Name the blood parasite species.
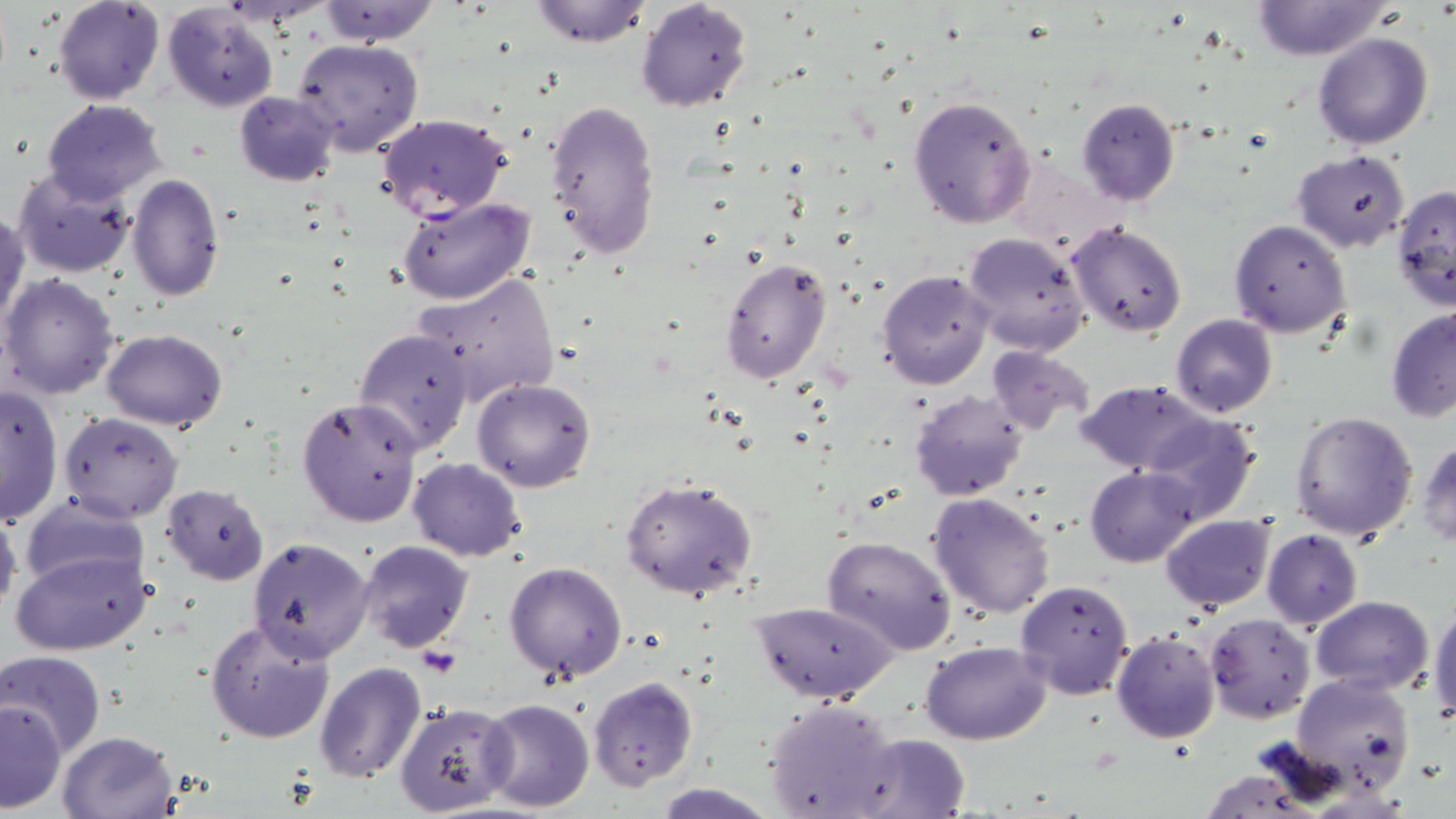

Plasmodium falciparum.

{
  "modality": "optical microscopy",
  "plasmodium_falciparum_infected_red_blood_cell_locations": "approximate bounding boxes as (x1, y1, x2, y2) in pixels: (374, 112, 513, 224)",
  "uninfected_red_blood_cell_locations": "approximate bounding boxes as (x1, y1, x2, y2) in pixels: (53, 0, 164, 104), (317, 0, 439, 46), (528, 0, 652, 48), (636, 0, 753, 113), (1249, 1, 1390, 61), (163, 3, 279, 112), (1312, 32, 1434, 150), (291, 38, 424, 157), (234, 90, 340, 186), (908, 95, 1036, 229), (41, 98, 167, 204), (1075, 98, 1181, 206), (545, 99, 663, 265), (1291, 149, 1411, 254), (1006, 159, 1125, 253), (13, 167, 138, 278), (127, 174, 224, 301), (1390, 186, 1455, 311), (396, 194, 536, 306), (0, 208, 28, 332), (1228, 218, 1352, 338), (1066, 222, 1188, 337), (964, 230, 1091, 354), (718, 255, 833, 386), (876, 268, 995, 390), (414, 269, 561, 407), (0, 272, 121, 401), (1386, 306, 1456, 421), (1171, 313, 1278, 418), (102, 328, 229, 431), (352, 328, 474, 456), (986, 344, 1095, 437), (472, 378, 597, 492), (1076, 381, 1210, 472), (0, 385, 64, 525), (908, 390, 1028, 501), (296, 396, 424, 528), (1289, 410, 1418, 542), (59, 411, 183, 523), (1140, 414, 1260, 526), (1416, 439, 1456, 548), (408, 456, 526, 562), (1087, 465, 1199, 566), (620, 478, 759, 601), (161, 483, 269, 584), (928, 491, 1056, 618), (18, 494, 148, 596), (0, 502, 22, 627), (1161, 514, 1275, 611), (1262, 529, 1363, 628), (823, 536, 956, 653), (248, 537, 374, 666), (356, 540, 473, 653), (10, 548, 152, 657), (504, 561, 629, 681), (1015, 579, 1135, 702), (1310, 595, 1432, 695), (750, 600, 895, 703), (1430, 601, 1456, 721), (1205, 614, 1316, 722), (206, 620, 337, 744), (1113, 631, 1220, 743), (922, 641, 1049, 745), (2, 650, 106, 758), (315, 663, 426, 783), (1292, 674, 1416, 796), (589, 676, 698, 791), (480, 698, 594, 814), (1, 699, 68, 813), (763, 700, 900, 818), (394, 702, 517, 817), (56, 731, 181, 819), (857, 733, 971, 818), (654, 783, 777, 818)",
  "magnification": "1000x",
  "image_size": "1456×819 pixels",
  "stain": "May-Grünwald-Giemsa",
  "preparation": "thin blood smear",
  "field_of_view": "single"
}